Report the malaria status of this cell.
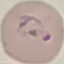

It is parasitized.

Acquired by smartphone through the microscope eyepiece. Giemsa-stained preparation. Automatically extracted cell patch, resized to 64 × 64 pixels. Thin blood film.